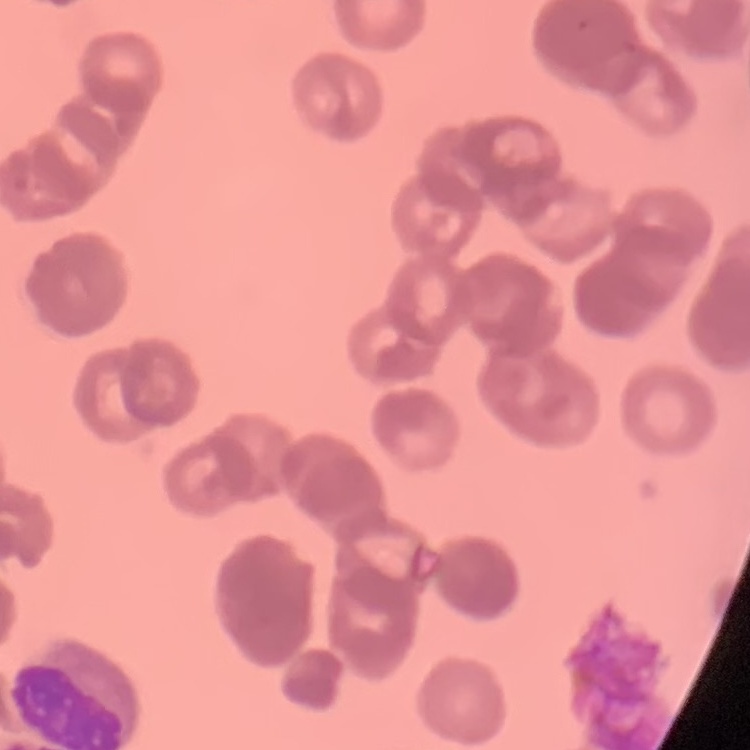
The erythrocytes exhibit rouleaux formation. Thin blood smear. Square crop of a larger photomicrograph. Stained with either Field's or Giemsa.